Give the location of every parasitized RBC.
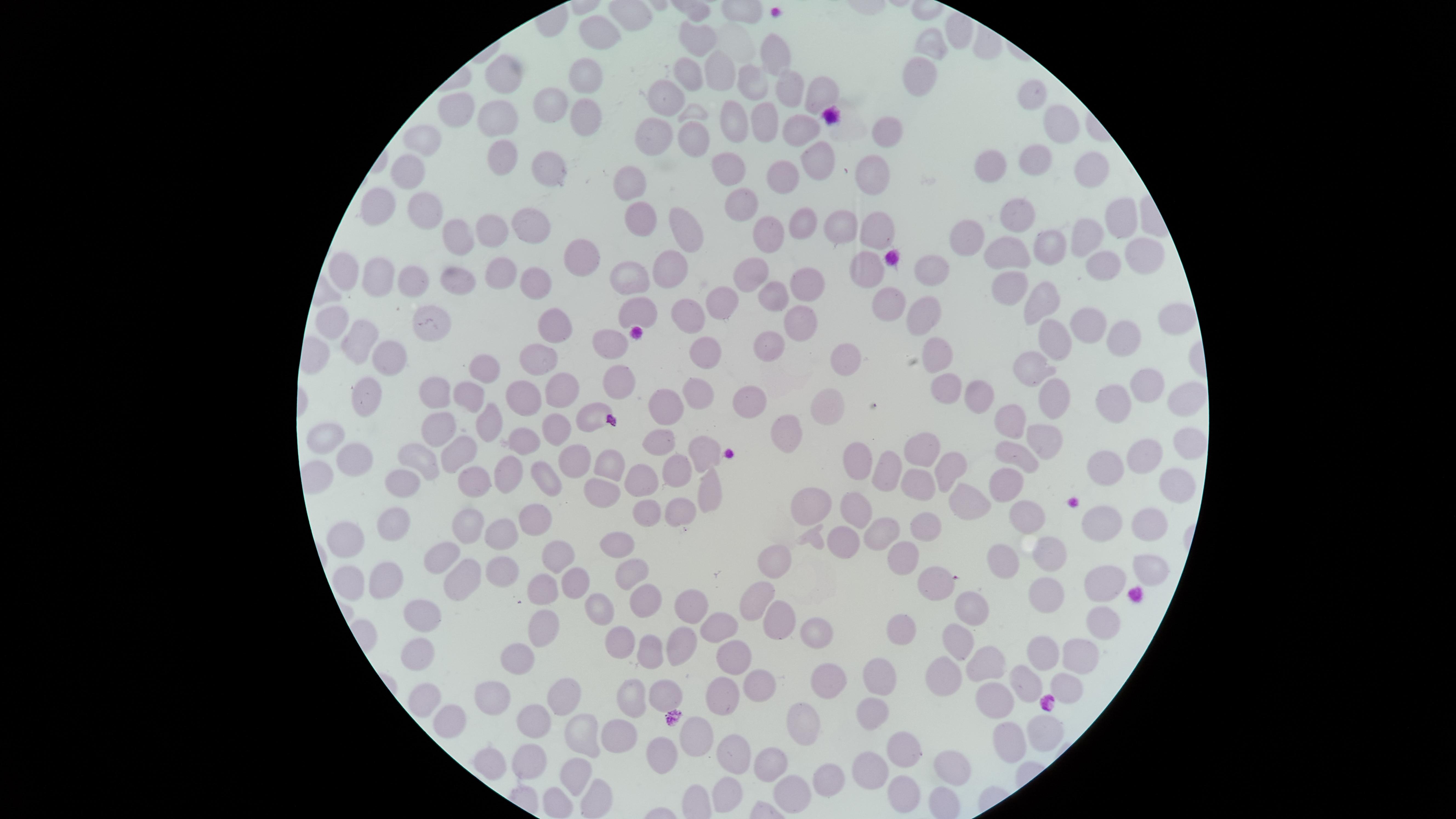
No parasitized RBCs identified.

Approximate marker points, in pixels from the top-left corner. Uninfected RBCs: (x=952, y=30), (x=603, y=31), (x=696, y=37), (x=931, y=44), (x=775, y=49), (x=501, y=70), (x=684, y=73), (x=588, y=74), (x=716, y=74), (x=913, y=75), (x=752, y=80), (x=786, y=87), (x=821, y=94), (x=1033, y=95), (x=554, y=96), (x=668, y=97), (x=464, y=103), (x=586, y=110), (x=494, y=115), (x=726, y=118), (x=765, y=119), (x=1057, y=122), (x=797, y=128), (x=885, y=128), (x=656, y=134), (x=690, y=135), (x=425, y=142), (x=1033, y=150), (x=499, y=151), (x=816, y=157), (x=724, y=158), (x=998, y=161), (x=549, y=169), (x=1093, y=169), (x=780, y=171), (x=410, y=173), (x=873, y=173), (x=622, y=178), (x=379, y=199), (x=738, y=203), (x=418, y=205), (x=639, y=217), (x=1020, y=218), (x=533, y=219), (x=799, y=220), (x=1114, y=220), (x=838, y=223), (x=874, y=226), (x=492, y=230), (x=772, y=231), (x=451, y=232), (x=688, y=232), (x=970, y=232), (x=1088, y=233), (x=1047, y=245), (x=1003, y=252), (x=1133, y=254), (x=580, y=257), (x=1100, y=261), (x=862, y=262), (x=350, y=267), (x=672, y=267), (x=747, y=268), (x=928, y=269), (x=378, y=273), (x=447, y=274), (x=489, y=275), (x=632, y=275), (x=411, y=281), (x=801, y=283), (x=537, y=285), (x=1005, y=287), (x=773, y=292), (x=1039, y=299), (x=716, y=303), (x=634, y=304), (x=892, y=304), (x=428, y=314), (x=918, y=314), (x=679, y=316), (x=336, y=318), (x=1174, y=320), (x=793, y=321), (x=1089, y=322), (x=556, y=330), (x=1125, y=333), (x=357, y=334), (x=1054, y=334), (x=607, y=340), (x=774, y=345), (x=936, y=347), (x=714, y=353), (x=390, y=355), (x=842, y=355), (x=1029, y=362), (x=535, y=363), (x=483, y=371), (x=621, y=376), (x=1142, y=376), (x=940, y=384), (x=1054, y=387), (x=562, y=388), (x=433, y=389), (x=360, y=391), (x=704, y=391), (x=977, y=393), (x=468, y=394), (x=518, y=396), (x=751, y=396), (x=1178, y=397), (x=1110, y=400), (x=663, y=402), (x=828, y=403), (x=590, y=414), (x=1009, y=418), (x=484, y=425), (x=788, y=425), (x=439, y=427), (x=553, y=430), (x=1043, y=433), (x=323, y=438), (x=527, y=439), (x=650, y=441), (x=922, y=445), (x=1189, y=445), (x=1148, y=446), (x=695, y=450), (x=460, y=454), (x=1009, y=455), (x=576, y=456), (x=857, y=456), (x=429, y=459), (x=358, y=460), (x=608, y=463), (x=891, y=464), (x=944, y=465), (x=1111, y=466), (x=678, y=467), (x=545, y=471), (x=640, y=473), (x=508, y=475), (x=1000, y=475), (x=470, y=478), (x=406, y=479), (x=921, y=480), (x=603, y=487), (x=1171, y=487), (x=709, y=491), (x=965, y=497), (x=813, y=498), (x=856, y=504), (x=678, y=509), (x=642, y=510), (x=1033, y=512), (x=536, y=515), (x=921, y=521), (x=465, y=522), (x=1142, y=523), (x=390, y=524), (x=1100, y=525), (x=881, y=528), (x=835, y=537), (x=498, y=538), (x=612, y=538), (x=342, y=540), (x=1004, y=554), (x=1047, y=554), (x=772, y=555), (x=563, y=556), (x=898, y=557), (x=440, y=559), (x=496, y=568), (x=1146, y=569), (x=621, y=572), (x=336, y=578), (x=454, y=579), (x=380, y=580), (x=946, y=580), (x=1106, y=581), (x=573, y=582), (x=546, y=587), (x=754, y=595), (x=640, y=598), (x=1049, y=598), (x=599, y=605), (x=693, y=609), (x=417, y=611), (x=973, y=612), (x=773, y=617), (x=1100, y=617), (x=717, y=628), (x=906, y=628), (x=541, y=629), (x=814, y=632), (x=612, y=637), (x=959, y=639), (x=681, y=645), (x=1077, y=646), (x=411, y=651), (x=1038, y=652), (x=652, y=654), (x=991, y=658), (x=512, y=659), (x=736, y=659), (x=945, y=671), (x=832, y=676), (x=878, y=678), (x=1024, y=679), (x=751, y=684), (x=498, y=686), (x=1068, y=686), (x=628, y=690), (x=426, y=694), (x=660, y=694), (x=722, y=695), (x=562, y=696), (x=1003, y=698), (x=865, y=709), (x=445, y=717), (x=532, y=723), (x=803, y=728), (x=616, y=731), (x=1041, y=732), (x=582, y=733), (x=703, y=738), (x=1011, y=740), (x=898, y=747), (x=658, y=749), (x=733, y=756), (x=490, y=757), (x=778, y=761), (x=531, y=763), (x=870, y=763), (x=948, y=764), (x=570, y=772), (x=821, y=775), (x=903, y=784), (x=784, y=791), (x=724, y=793), (x=594, y=794). Smartphone photograph through the microscope eyepiece. Circular visible region. One field of view of the specimen. Thin blood smear. Image is 1456×819 pixels. Giemsa stain.